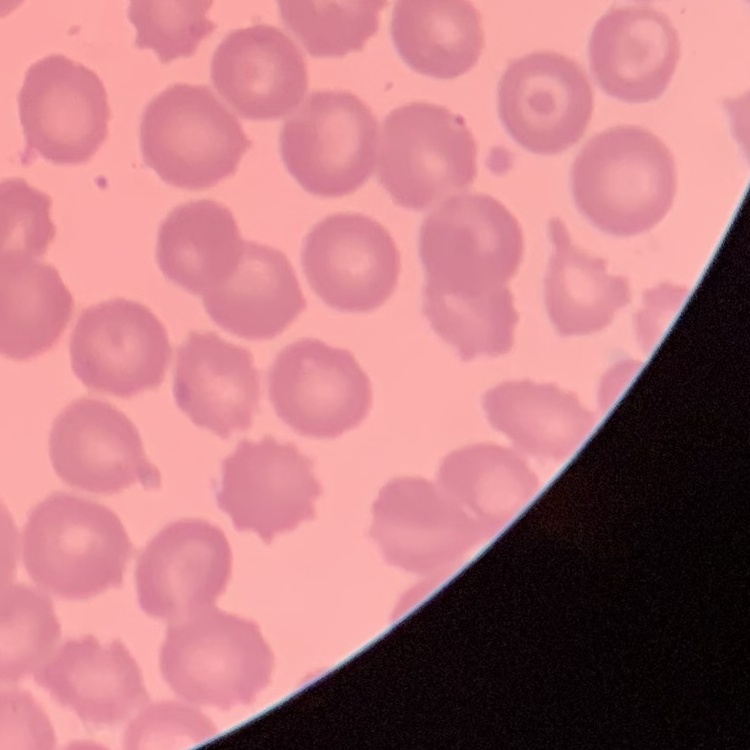

Summary:
  - Red blood cell morphology: no rouleaux formation
  - Stain: Field's or Giemsa
  - Preparation: thin blood smear
  - Image type: one tile cut from a larger photomicrograph